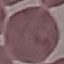

result: no malaria parasites seen
image_type: cell patch, automatically extracted from a larger field of view and resized to 64 × 64 pixels
preparation: thin blood film
capture: smartphone camera at the microscope eyepiece
stain: Giemsa